Locate and identify every blood parasite.
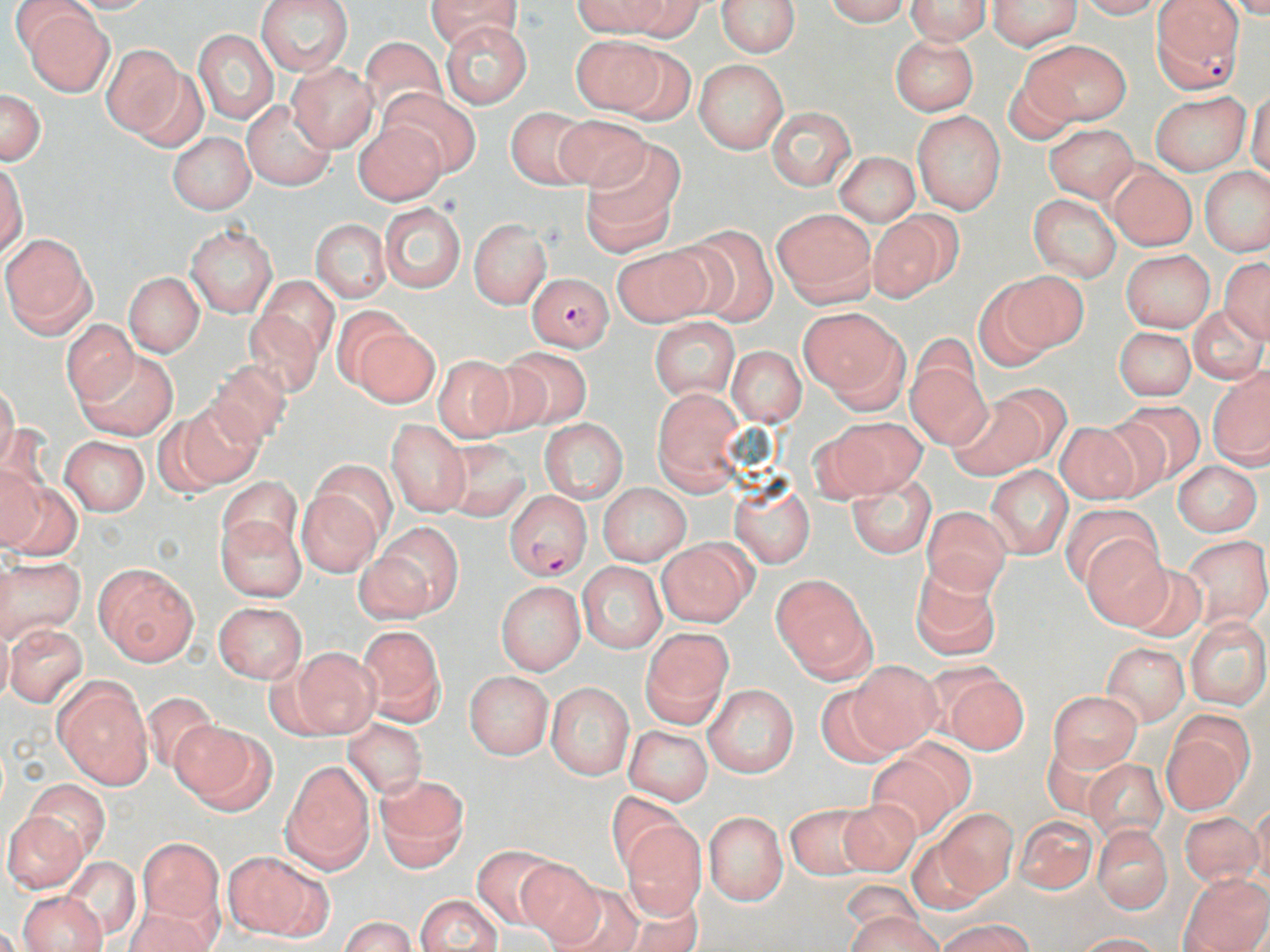
Approximate bounding boxes as (x1,y1)-(x2,y2) corner pairs in pixels.
Plasmodium falciparum-infected red blood cells: (1152,0)-(1245,91), (527,272)-(613,351), (506,491)-(591,581).
No Plasmodium ovale, Plasmodium malariae, Plasmodium vivax, Babesia divergens, or Trypanosoma brucei observed.

{
  "slide_level_diagnosis": "Plasmodium falciparum",
  "stain": "May-Grünwald-Giemsa",
  "image_size": "1270×952 pixels",
  "magnification": "1000x",
  "field_of_view": "one of a larger specimen",
  "preparation": "thin blood film",
  "modality": "light microscopy",
  "uninfected_red_blood_cell_locations": "approximate bounding boxes as (x1,y1)-(x2,y2) corner pairs in pixels: (62,0)-(157,14), (256,0)-(355,76), (425,0)-(524,50), (573,0)-(672,36), (620,0)-(706,38), (716,0)-(799,57), (822,0)-(913,25), (906,0)-(991,45), (987,0)-(1082,51), (1074,0)-(1163,19), (1222,0)-(1270,18), (7,2)-(97,63), (20,8)-(114,95), (441,21)-(532,108), (194,29)-(278,123), (568,34)-(669,114), (890,35)-(979,115), (357,36)-(447,124), (1022,39)-(1131,127), (611,43)-(696,125), (102,45)-(189,141), (693,58)-(788,154), (285,61)-(377,152), (1246,87)-(1269,180), (383,89)-(478,175), (1,90)-(46,165), (1150,91)-(1252,174), (243,99)-(336,190), (766,105)-(857,191), (505,106)-(594,189), (912,110)-(1005,214), (554,113)-(652,194), (354,121)-(446,204), (1043,123)-(1139,201), (168,133)-(255,213), (580,146)-(682,256), (834,151)-(921,225), (1107,164)-(1198,251), (1,165)-(27,256), (1200,167)-(1269,255), (1029,194)-(1122,281), (379,202)-(467,294), (772,209)-(876,305), (867,211)-(959,302), (310,218)-(391,304), (468,219)-(551,309), (675,225)-(781,326), (186,226)-(276,318), (1,233)-(95,336), (610,244)-(714,328), (1121,250)-(1215,332), (1220,258)-(1270,341), (123,271)-(205,357), (994,271)-(1087,357), (251,280)-(336,379), (973,284)-(1058,373), (1187,304)-(1267,385), (330,306)-(416,392), (799,307)-(908,406), (650,318)-(740,399), (61,322)-(138,402), (352,325)-(440,408), (1114,327)-(1196,401), (496,346)-(594,430), (728,346)-(806,426), (75,349)-(178,441), (907,354)-(992,450), (433,356)-(517,442), (206,360)-(293,447), (1207,367)-(1269,469), (0,383)-(19,472), (653,388)-(745,492), (947,392)-(1047,480), (172,400)-(263,489), (1113,400)-(1207,485), (822,418)-(925,498), (385,419)-(470,517), (539,420)-(627,502), (1052,420)-(1152,505), (60,436)-(150,515), (440,437)-(532,521), (0,460)-(44,552), (307,460)-(397,548), (1173,461)-(1262,536), (986,466)-(1072,558), (847,471)-(935,559), (2,476)-(79,561), (216,477)-(303,558), (729,481)-(814,567), (296,484)-(385,576), (598,484)-(690,565), (1060,502)-(1160,589), (921,505)-(1011,593), (215,511)-(307,602), (373,523)-(463,616), (1182,534)-(1270,628), (1082,536)-(1171,627), (658,539)-(755,627), (352,551)-(433,625), (1111,555)-(1203,640), (0,557)-(85,644), (577,562)-(666,654), (910,562)-(1002,662), (94,563)-(199,665), (770,576)-(876,680), (495,581)-(586,676), (212,601)-(307,683), (1184,618)-(1270,709), (5,623)-(89,707), (357,624)-(446,725), (640,627)-(732,727), (1102,643)-(1188,726), (287,646)-(380,738), (846,659)-(943,753), (935,669)-(1030,756), (465,672)-(553,759), (53,676)-(153,789), (546,681)-(634,779), (703,683)-(799,776), (814,683)-(902,767), (139,690)-(220,774), (1049,690)-(1141,771), (1162,714)-(1252,813), (344,719)-(428,799), (170,721)-(272,811), (624,725)-(713,806), (867,752)-(961,840), (1083,757)-(1167,842), (282,760)-(374,872), (374,773)-(471,873), (24,781)-(110,861), (606,791)-(685,873), (835,798)-(923,877), (1249,803)-(1270,892), (785,804)-(873,881), (933,809)-(1017,898), (1,810)-(87,893), (1180,810)-(1264,888), (704,811)-(788,904), (1014,817)-(1098,896), (621,820)-(707,919), (1091,824)-(1172,913), (907,833)-(992,914), (135,838)-(224,931), (471,845)-(564,931), (225,850)-(329,940), (61,856)-(141,940), (513,857)-(606,947), (1179,872)-(1270,952), (839,880)-(929,944), (544,882)-(645,952), (18,891)-(106,952), (415,894)-(504,952), (615,898)-(704,952), (125,901)-(218,952), (845,909)-(940,952), (341,917)-(417,952), (938,918)-(1033,952), (1071,933)-(1165,952)"
}